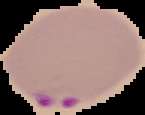
{
  "image_type": "segmented cell region on a black background",
  "image_size": "145×115 pixels",
  "preparation": "thin blood film",
  "malaria_status": "parasitized"
}